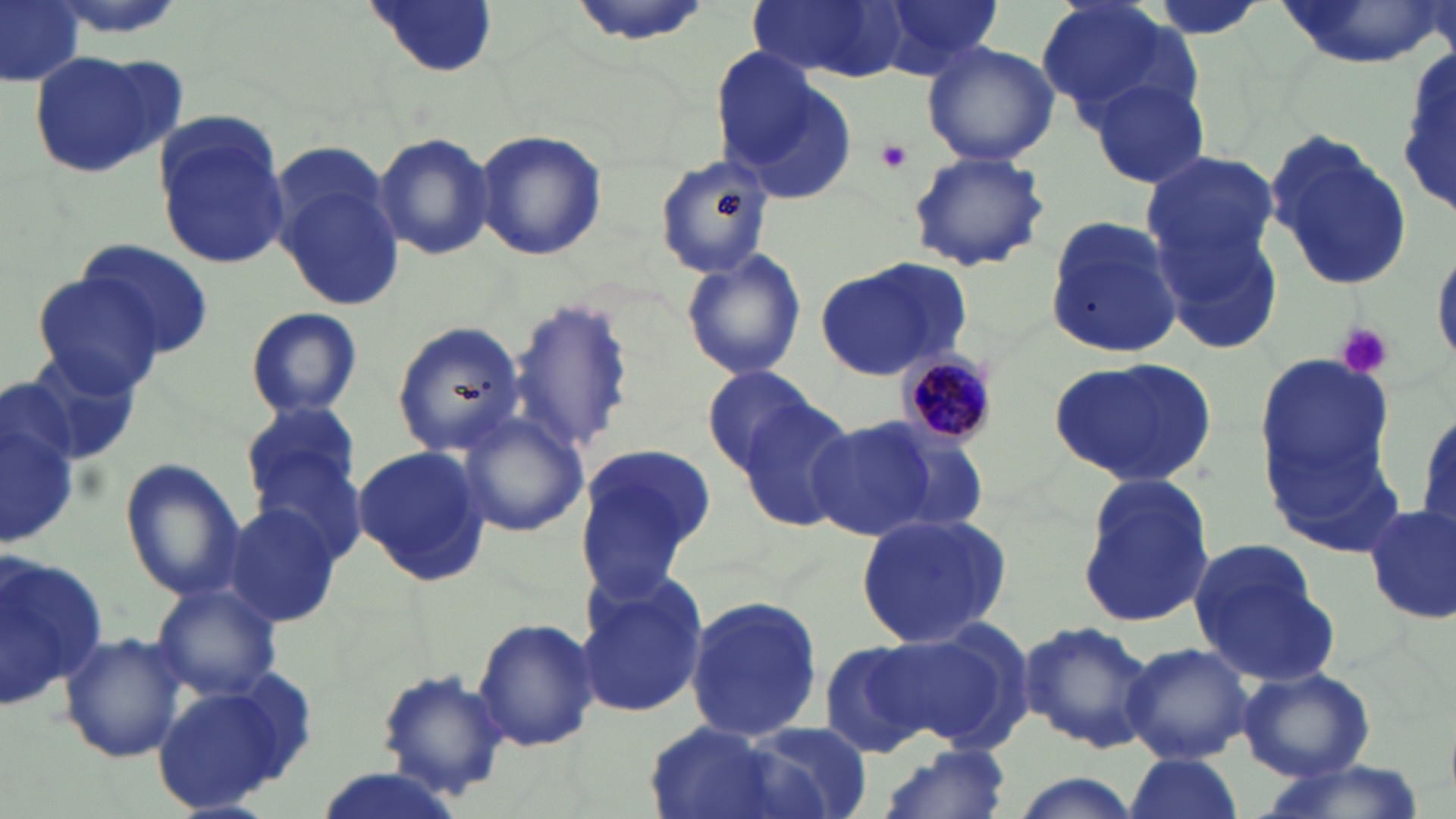
slide-level diagnosis = Plasmodium malariae
magnification = 1000x
image size = 1456×819 pixels
uninfected red blood cell locations = approximate bounding boxes as (x1, y1, x2, y2) in pixels: (0, 0, 84, 89), (364, 0, 498, 80), (564, 0, 714, 47), (748, 0, 909, 82), (873, 0, 1007, 78), (1035, 0, 1199, 126), (1277, 0, 1442, 67), (1398, 36, 1456, 229), (920, 40, 1059, 167), (706, 45, 823, 174), (26, 49, 179, 178), (1083, 69, 1213, 193), (727, 74, 858, 204), (154, 115, 291, 271), (474, 128, 608, 261), (372, 130, 495, 260), (1265, 132, 1414, 292), (1140, 148, 1280, 279), (906, 150, 1052, 273), (653, 151, 777, 278), (271, 168, 407, 312), (1044, 217, 1187, 360), (1160, 217, 1285, 357), (74, 238, 216, 362), (1428, 243, 1456, 370), (679, 247, 807, 382), (814, 258, 971, 382), (29, 272, 168, 396), (509, 296, 634, 458), (244, 306, 363, 419), (391, 321, 525, 458), (1255, 349, 1395, 514), (25, 350, 148, 468), (1052, 355, 1218, 488), (702, 364, 823, 472), (3, 387, 82, 549), (735, 398, 858, 531), (241, 401, 365, 523), (1409, 402, 1456, 540), (453, 410, 590, 539), (803, 416, 934, 540), (870, 418, 990, 534), (574, 442, 717, 600), (351, 445, 489, 584), (121, 458, 245, 599), (1076, 473, 1216, 629), (221, 504, 343, 626), (1363, 505, 1454, 627), (855, 512, 1012, 648), (1, 545, 105, 707), (1189, 547, 1335, 686), (575, 572, 709, 719), (150, 581, 282, 700), (684, 593, 824, 745), (472, 616, 600, 754), (871, 619, 1033, 753), (1020, 619, 1157, 755), (60, 631, 190, 762), (818, 639, 943, 762), (1122, 640, 1254, 764), (374, 662, 511, 799), (1241, 667, 1375, 780), (152, 674, 313, 813), (737, 722, 876, 817), (640, 723, 798, 819), (877, 741, 1013, 819), (1124, 753, 1241, 819), (1251, 761, 1425, 819), (306, 768, 469, 819), (1006, 773, 1142, 819)
preparation = thin blood smear
platelet locations = approximate bounding boxes as (x1, y1, x2, y2) in pixels: (876, 139, 913, 175), (1332, 321, 1394, 379)
Plasmodium malariae-infected red blood cell locations = approximate bounding boxes as (x1, y1, x2, y2) in pixels: (898, 352, 997, 446)
stain = May-Grünwald-Giemsa
field of view = one of a larger specimen
modality = light microscopy